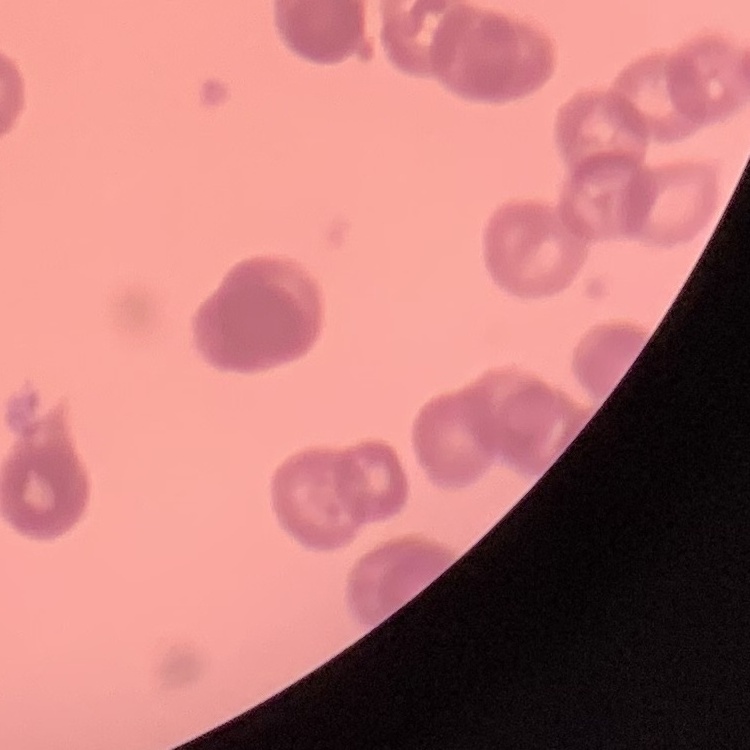 The red blood cells exhibit rouleaux formation. Thin blood smear. Field's or Giemsa stain. One tile cut from a larger photomicrograph.